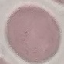

Summary:
  - Malaria status: uninfected
  - Capture: smartphone through the microscope eyepiece
  - Image type: automatically extracted cell patch, resized to 64 × 64 pixels
  - Stain: Giemsa
  - Preparation: thin blood smear